Assess this cell for malaria.
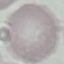

It is uninfected.

Acquired by smartphone through the microscope eyepiece. Automatically extracted cell patch, resized to 64 × 64 pixels. Giemsa-stained preparation. Thin smear of blood.